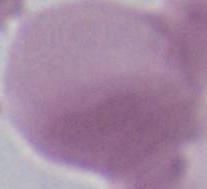

An erythrocyte is shown. 1000x magnification. Photomicrograph.